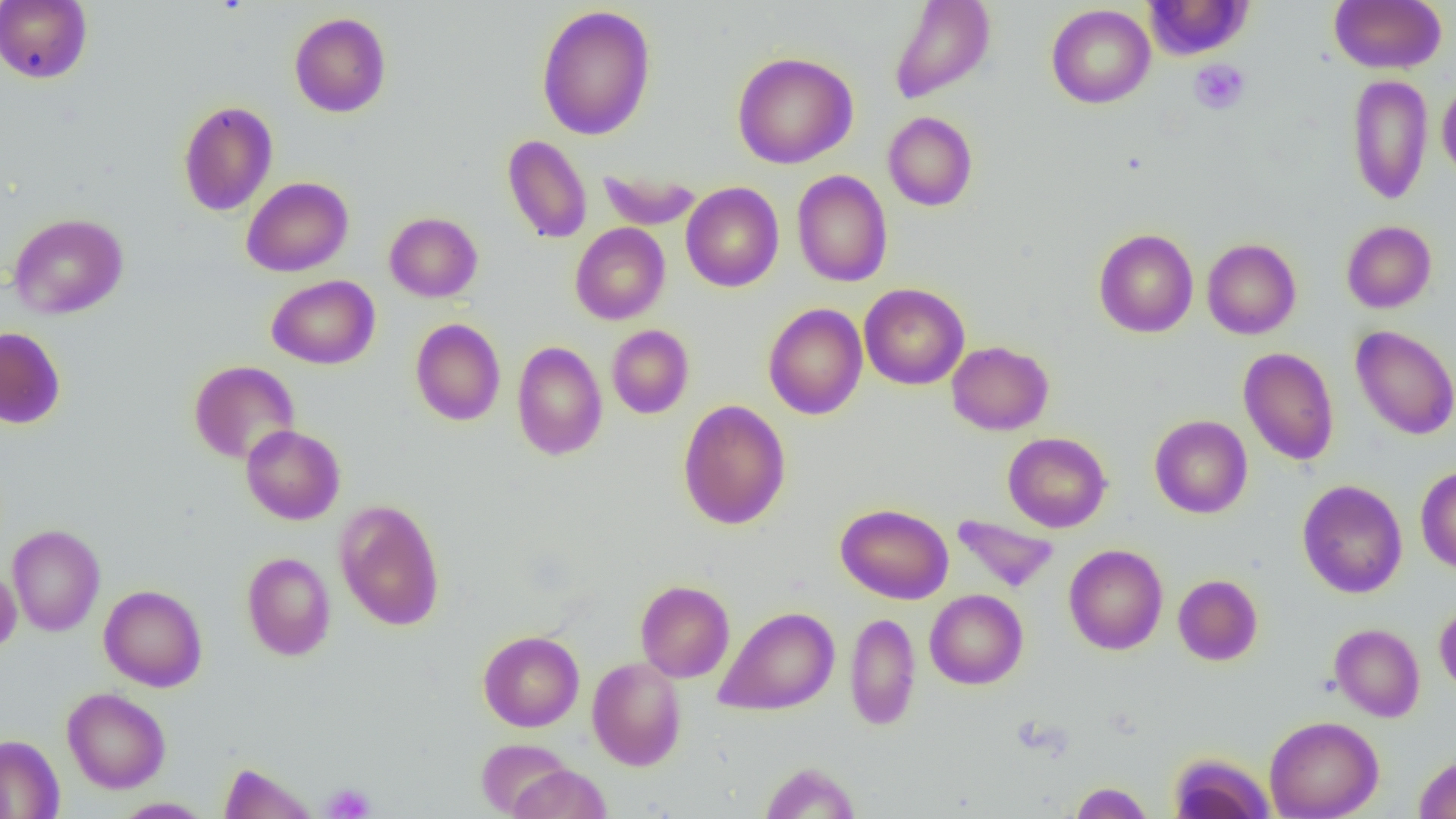
Summary:
  - Coordinate format: approximate bounding boxes as (x1,y1)-(x2,y2) corner pairs in pixels
  - Uninfected red blood cell locations: (888,0)-(995,104), (1143,0)-(1253,60), (1329,0)-(1446,74), (0,1)-(92,84), (536,4)-(656,141), (1046,4)-(1155,108), (289,12)-(391,117), (732,51)-(858,169), (1347,74)-(1433,205), (1437,81)-(1456,182), (178,100)-(278,216), (883,111)-(978,211), (502,134)-(592,244), (599,168)-(701,230), (791,170)-(892,287), (242,177)-(354,277), (681,182)-(784,292), (384,212)-(482,302), (8,213)-(128,319), (1342,220)-(1436,313), (570,223)-(670,325), (1093,228)-(1198,338), (1202,238)-(1301,339), (266,275)-(380,369), (859,283)-(969,390), (764,303)-(867,420), (410,318)-(506,425), (607,325)-(694,419), (1351,325)-(1456,440), (0,326)-(66,429), (512,341)-(607,460), (946,341)-(1053,435), (1238,347)-(1339,465), (189,360)-(300,464), (678,399)-(791,530), (1150,415)-(1252,518), (241,424)-(345,525), (1003,432)-(1111,532), (1415,466)-(1456,573), (1297,479)-(1407,598), (335,500)-(445,631), (836,503)-(953,604), (952,514)-(1059,593), (7,524)-(105,636), (1063,544)-(1168,655), (242,552)-(336,661), (0,567)-(21,654), (1173,574)-(1263,665), (635,580)-(735,682), (99,585)-(207,691), (925,589)-(1028,689), (1435,601)-(1456,696), (715,605)-(840,716), (845,612)-(921,731), (1329,623)-(1425,721), (478,630)-(584,732), (587,657)-(686,771), (62,687)-(171,793), (1264,715)-(1384,819), (0,734)-(65,818), (476,740)-(572,817), (1167,752)-(1275,819), (1414,753)-(1456,818), (759,761)-(859,819), (217,762)-(318,819), (508,764)-(612,819), (1069,782)-(1154,818), (112,797)-(214,818)
  - Platelet locations: (1189,59)-(1250,114), (321,783)-(375,818)
  - Slide-level diagnosis: negative for blood parasites
  - Modality: optical microscopy
  - Preparation: thin blood film
  - Image size: 1456×819 pixels
  - Field of view: one of a larger specimen
  - Magnification: 1000x